Locate and identify every blood parasite.
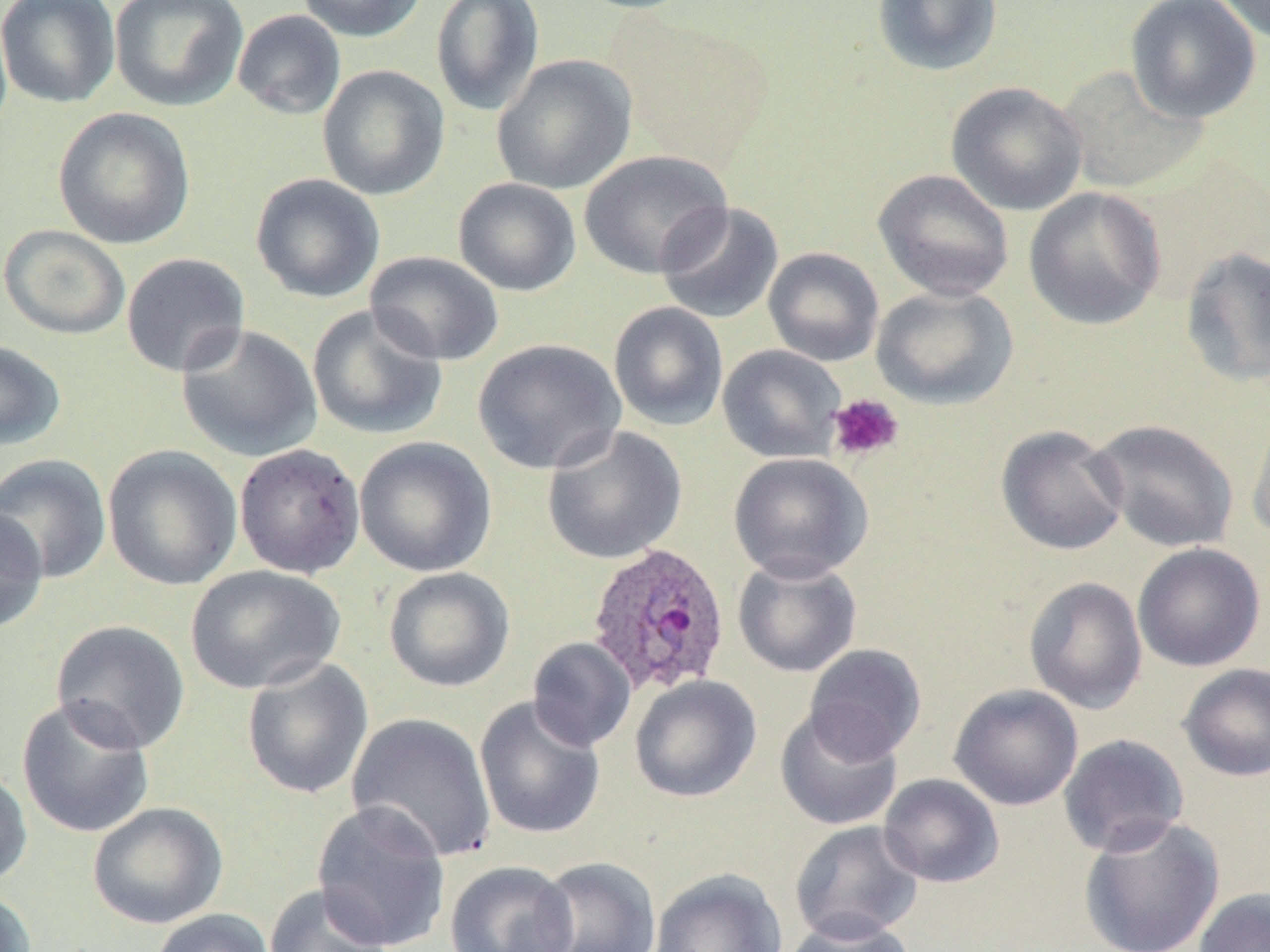
Approximate bounding boxes as named x1/y1/x2/y2 corners in pixels.
Plasmodium ovale-infected red blood cells: (x1=586, y1=541, x2=732, y2=695).
No Plasmodium falciparum, Plasmodium malariae, Plasmodium vivax, Babesia divergens, or Trypanosoma brucei observed.

slide-level diagnosis = Plasmodium ovale
field of view = one of a larger specimen
modality = optical microscopy
magnification = 1000x
image size = 1270×952 pixels
preparation = thin blood smear
uninfected red blood cell locations = approximate bounding boxes as named x1/y1/x2/y2 corners in pixels: (x1=0, y1=0, x2=120, y2=108), (x1=110, y1=0, x2=248, y2=111), (x1=296, y1=0, x2=428, y2=43), (x1=567, y1=0, x2=705, y2=15), (x1=871, y1=0, x2=1004, y2=77), (x1=1123, y1=0, x2=1262, y2=124), (x1=1214, y1=0, x2=1269, y2=44), (x1=431, y1=1, x2=545, y2=116), (x1=232, y1=9, x2=346, y2=120), (x1=614, y1=15, x2=773, y2=171), (x1=491, y1=54, x2=637, y2=195), (x1=317, y1=64, x2=450, y2=201), (x1=1056, y1=65, x2=1208, y2=195), (x1=946, y1=81, x2=1087, y2=216), (x1=52, y1=107, x2=196, y2=250), (x1=579, y1=150, x2=731, y2=279), (x1=873, y1=168, x2=1014, y2=302), (x1=250, y1=173, x2=385, y2=303), (x1=453, y1=177, x2=582, y2=297), (x1=1023, y1=187, x2=1166, y2=330), (x1=655, y1=202, x2=784, y2=325), (x1=1, y1=224, x2=131, y2=340), (x1=763, y1=247, x2=884, y2=367), (x1=1179, y1=247, x2=1270, y2=387), (x1=365, y1=251, x2=504, y2=365), (x1=120, y1=252, x2=251, y2=378), (x1=871, y1=285, x2=1018, y2=409), (x1=608, y1=301, x2=729, y2=431), (x1=307, y1=304, x2=448, y2=441), (x1=176, y1=323, x2=324, y2=462), (x1=472, y1=338, x2=626, y2=475), (x1=0, y1=340, x2=66, y2=451), (x1=717, y1=344, x2=847, y2=463), (x1=1248, y1=404, x2=1270, y2=543), (x1=1088, y1=418, x2=1240, y2=553), (x1=995, y1=424, x2=1130, y2=556), (x1=542, y1=425, x2=687, y2=565), (x1=353, y1=436, x2=498, y2=577), (x1=233, y1=443, x2=366, y2=580), (x1=102, y1=444, x2=243, y2=591), (x1=728, y1=452, x2=873, y2=582), (x1=0, y1=453, x2=112, y2=584), (x1=0, y1=506, x2=48, y2=633), (x1=1132, y1=542, x2=1266, y2=672), (x1=732, y1=554, x2=863, y2=678), (x1=185, y1=565, x2=346, y2=695), (x1=383, y1=567, x2=515, y2=692), (x1=1023, y1=576, x2=1148, y2=715), (x1=50, y1=619, x2=190, y2=754), (x1=527, y1=637, x2=636, y2=752), (x1=803, y1=644, x2=926, y2=763), (x1=241, y1=657, x2=374, y2=800), (x1=1177, y1=662, x2=1270, y2=782), (x1=630, y1=675, x2=761, y2=803), (x1=948, y1=684, x2=1084, y2=811), (x1=16, y1=696, x2=156, y2=839), (x1=474, y1=696, x2=606, y2=840), (x1=774, y1=706, x2=904, y2=832), (x1=346, y1=713, x2=497, y2=862), (x1=1057, y1=733, x2=1190, y2=857), (x1=0, y1=763, x2=33, y2=889), (x1=878, y1=773, x2=1004, y2=888), (x1=311, y1=801, x2=452, y2=952), (x1=87, y1=802, x2=228, y2=930), (x1=1077, y1=815, x2=1226, y2=952), (x1=789, y1=820, x2=925, y2=944), (x1=532, y1=856, x2=662, y2=951), (x1=443, y1=860, x2=578, y2=952), (x1=650, y1=869, x2=787, y2=952), (x1=263, y1=884, x2=393, y2=952), (x1=0, y1=887, x2=38, y2=952), (x1=1193, y1=887, x2=1270, y2=952), (x1=149, y1=909, x2=275, y2=952), (x1=781, y1=914, x2=917, y2=952)
platelet locations = approximate bounding boxes as named x1/y1/x2/y2 corners in pixels: (x1=826, y1=393, x2=905, y2=463)
stain = May-Grünwald-Giemsa